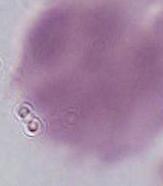
modality = micrograph
identification = red blood cell
magnification = 1000x